State the blood parasite species.
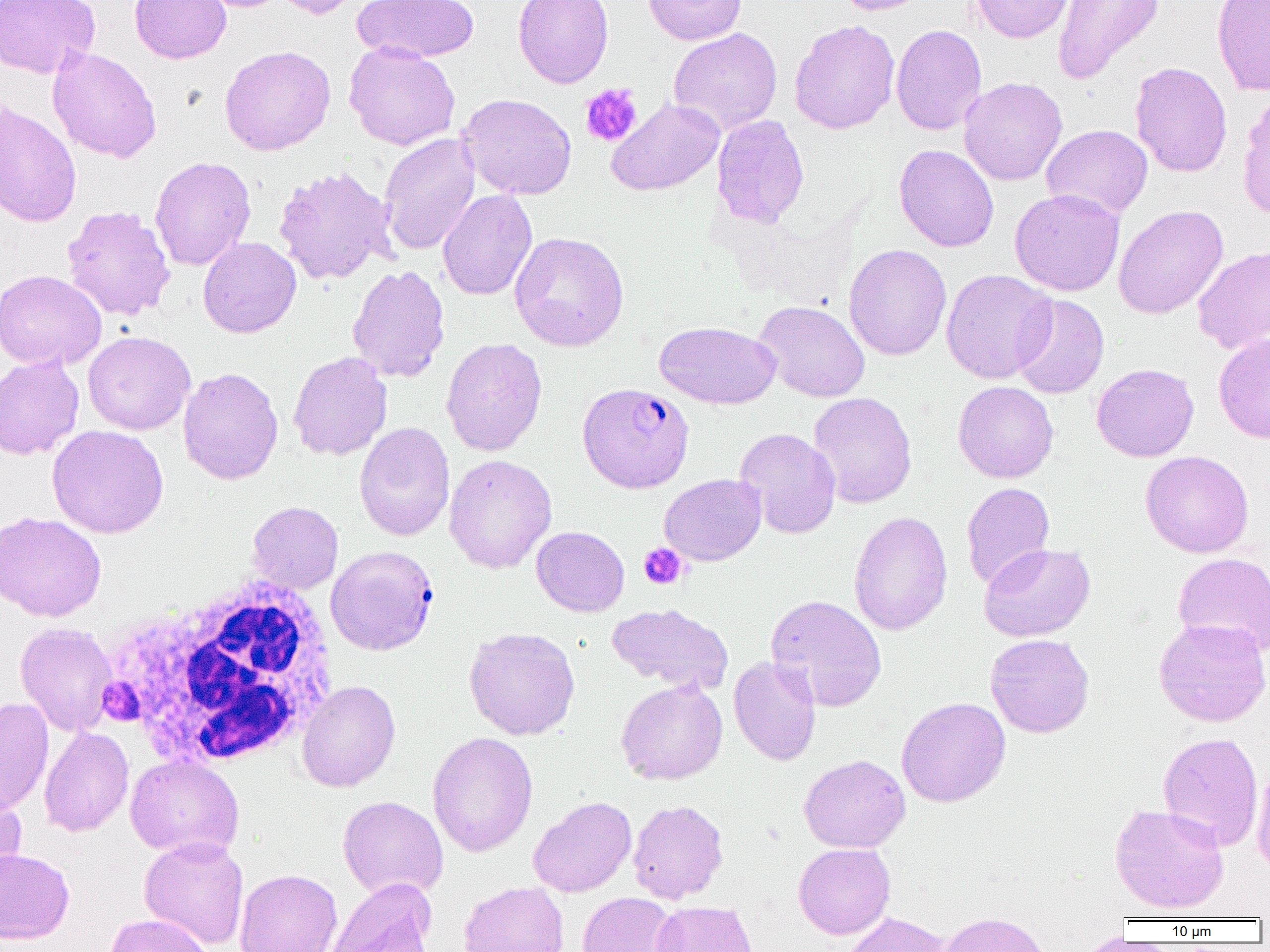
Plasmodium falciparum.

field of view = single
uninfected red blood cell locations = approximate bounding boxes as [x1, y1, x2, y2] in pixels: [0, 0, 100, 79], [129, 0, 231, 64], [270, 0, 365, 19], [353, 0, 479, 62], [513, 0, 614, 88], [644, 0, 746, 45], [833, 0, 936, 15], [971, 0, 1074, 43], [1052, 0, 1164, 85], [1211, 0, 1270, 96], [789, 19, 900, 134], [891, 24, 986, 135], [668, 27, 782, 135], [343, 42, 461, 150], [219, 45, 336, 155], [47, 46, 162, 163], [1130, 62, 1232, 177], [958, 77, 1068, 185], [1237, 92, 1270, 222], [457, 93, 578, 200], [606, 99, 724, 196], [0, 101, 82, 228], [711, 114, 810, 228], [1041, 124, 1153, 220], [379, 133, 480, 255], [894, 144, 999, 252], [150, 156, 256, 271], [273, 166, 397, 285], [1009, 188, 1125, 296], [437, 189, 537, 301], [61, 205, 176, 321], [1113, 205, 1228, 319], [509, 231, 630, 351], [198, 236, 302, 338], [844, 244, 951, 360], [1193, 245, 1270, 354], [347, 264, 450, 382], [0, 269, 107, 371], [941, 269, 1057, 383], [1010, 294, 1109, 398], [753, 300, 871, 402], [654, 321, 781, 409], [82, 331, 196, 435], [1213, 333, 1270, 444], [440, 337, 547, 456], [288, 351, 393, 460], [0, 354, 85, 459], [1091, 363, 1199, 462], [178, 366, 283, 485], [953, 381, 1058, 483], [808, 392, 917, 509], [354, 422, 455, 542], [47, 425, 169, 538], [734, 427, 841, 538], [1140, 450, 1254, 558], [443, 454, 557, 573], [659, 473, 766, 566], [961, 482, 1055, 589], [247, 501, 343, 593], [849, 510, 952, 636], [0, 511, 106, 621], [531, 526, 629, 617], [979, 543, 1095, 642], [1172, 552, 1270, 657], [765, 594, 887, 712], [607, 603, 734, 693], [1153, 618, 1270, 727], [15, 622, 118, 736], [464, 627, 581, 740], [985, 633, 1094, 738], [729, 655, 821, 766], [296, 680, 400, 792], [616, 680, 727, 784], [896, 697, 1010, 807], [0, 698, 54, 817], [39, 726, 134, 837], [427, 731, 538, 858], [1158, 731, 1263, 851], [125, 754, 244, 859], [799, 754, 910, 853], [1251, 763, 1270, 874], [0, 789, 27, 887], [337, 796, 448, 900], [528, 796, 637, 898], [628, 799, 728, 903], [1109, 803, 1230, 914], [139, 837, 249, 948], [793, 843, 895, 939], [0, 848, 75, 944], [235, 869, 342, 952], [323, 878, 437, 952], [458, 882, 569, 952], [576, 892, 679, 952], [650, 901, 758, 952], [840, 911, 956, 951], [938, 911, 1053, 952], [104, 913, 214, 952]
magnification = 1000x
white blood cell locations = approximate bounding boxes as [x1, y1, x2, y2] in pixels: [107, 574, 339, 770]
Plasmodium falciparum-infected red blood cell locations = approximate bounding boxes as [x1, y1, x2, y2] in pixels: [577, 382, 695, 493], [326, 546, 438, 655]
preparation = thin blood film
modality = optical microscopy
platelet locations = approximate bounding boxes as [x1, y1, x2, y2] in pixels: [580, 83, 643, 147], [639, 543, 688, 590], [97, 677, 142, 725]
image size = 1270×952 pixels